Assess this cell for malaria.
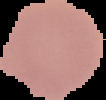
Uninfected.

{
  "image_size": "106×100 pixels",
  "image_type": "segmented cell region on a black background",
  "preparation": "thin blood film"
}